Assess this cell for malaria.
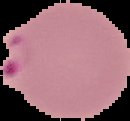
Parasitized.

Summary:
  - Image type: segmented cell region with the area outside set to black
  - Image size: 130×121 pixels
  - Preparation: thin blood film